Locate every uninfected red blood cell.
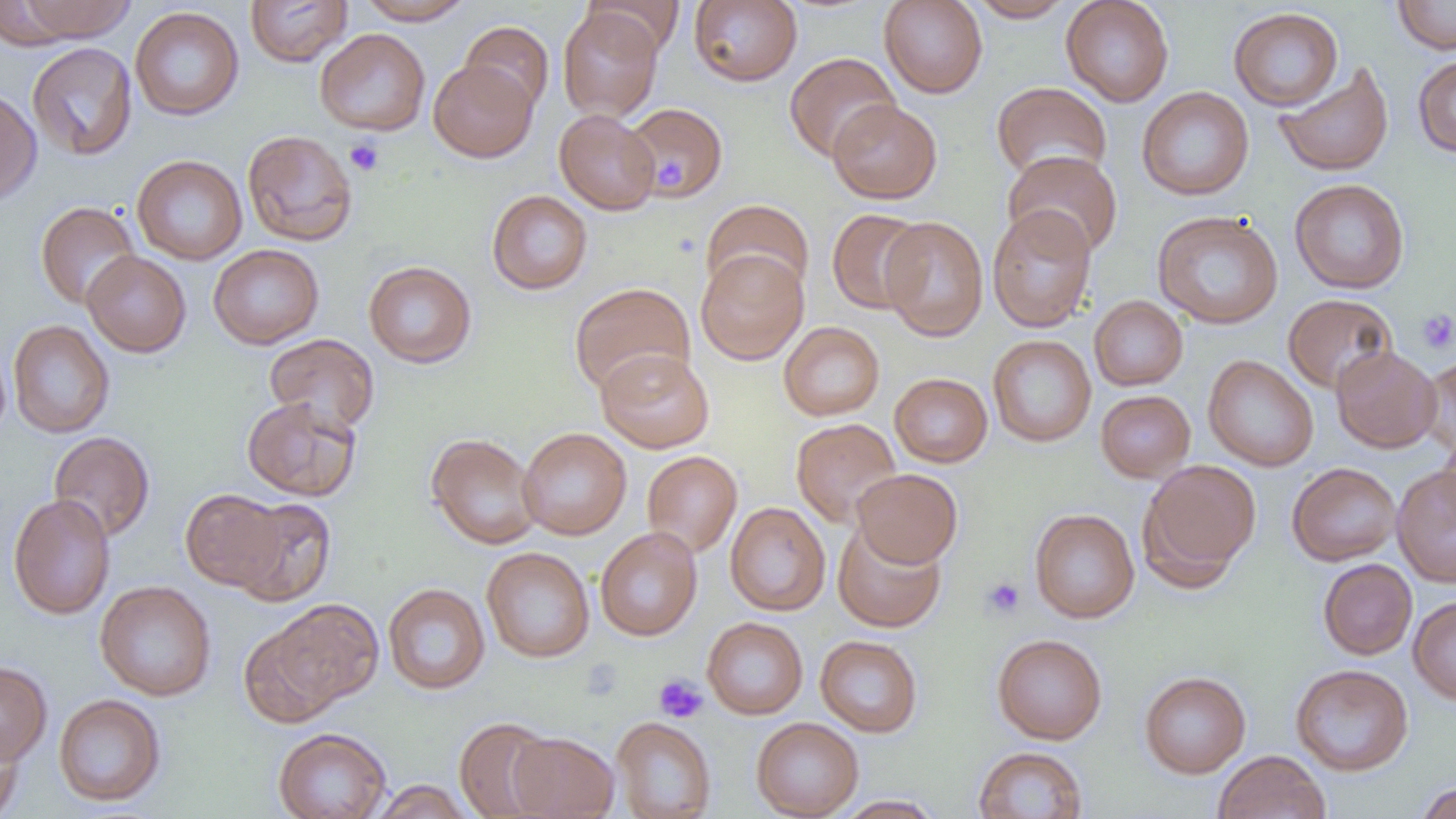

Approximate bounding boxes as named x1/y1/x2/y2 corners in pixels.
Uninfected red blood cells: (x1=13, y1=0, x2=136, y2=42), (x1=245, y1=0, x2=353, y2=67), (x1=357, y1=0, x2=475, y2=25), (x1=583, y1=0, x2=684, y2=56), (x1=688, y1=0, x2=802, y2=87), (x1=879, y1=0, x2=988, y2=99), (x1=967, y1=0, x2=1077, y2=22), (x1=1061, y1=0, x2=1174, y2=107), (x1=1392, y1=0, x2=1456, y2=54), (x1=129, y1=6, x2=244, y2=121), (x1=557, y1=6, x2=664, y2=121), (x1=1228, y1=6, x2=1344, y2=111), (x1=460, y1=20, x2=555, y2=116), (x1=315, y1=28, x2=430, y2=136), (x1=26, y1=42, x2=137, y2=161), (x1=784, y1=52, x2=901, y2=162), (x1=1412, y1=55, x2=1456, y2=157), (x1=428, y1=59, x2=538, y2=162), (x1=1274, y1=62, x2=1394, y2=177), (x1=992, y1=81, x2=1112, y2=182), (x1=1137, y1=86, x2=1254, y2=201), (x1=0, y1=88, x2=42, y2=206), (x1=828, y1=99, x2=942, y2=204), (x1=624, y1=102, x2=728, y2=201), (x1=554, y1=109, x2=661, y2=215), (x1=242, y1=130, x2=358, y2=246), (x1=1002, y1=150, x2=1123, y2=259), (x1=132, y1=155, x2=247, y2=265), (x1=1290, y1=178, x2=1410, y2=294), (x1=487, y1=190, x2=593, y2=294), (x1=700, y1=198, x2=814, y2=299), (x1=35, y1=201, x2=141, y2=310), (x1=987, y1=205, x2=1097, y2=333), (x1=826, y1=208, x2=928, y2=315), (x1=1152, y1=210, x2=1283, y2=329), (x1=879, y1=216, x2=989, y2=342), (x1=209, y1=244, x2=324, y2=349), (x1=696, y1=249, x2=808, y2=364), (x1=81, y1=251, x2=192, y2=357), (x1=363, y1=260, x2=477, y2=368), (x1=569, y1=282, x2=695, y2=396), (x1=1282, y1=293, x2=1398, y2=394), (x1=1089, y1=295, x2=1188, y2=390), (x1=8, y1=320, x2=115, y2=438), (x1=779, y1=321, x2=885, y2=420), (x1=264, y1=333, x2=380, y2=434), (x1=988, y1=335, x2=1096, y2=447), (x1=1331, y1=345, x2=1441, y2=453), (x1=596, y1=348, x2=714, y2=453), (x1=1203, y1=355, x2=1318, y2=471), (x1=1417, y1=355, x2=1456, y2=459), (x1=889, y1=373, x2=992, y2=467), (x1=1095, y1=390, x2=1196, y2=483), (x1=241, y1=396, x2=362, y2=501), (x1=790, y1=418, x2=902, y2=528), (x1=518, y1=427, x2=632, y2=540), (x1=1437, y1=429, x2=1456, y2=530), (x1=48, y1=431, x2=155, y2=541), (x1=425, y1=433, x2=543, y2=550), (x1=641, y1=451, x2=742, y2=558), (x1=1138, y1=458, x2=1260, y2=589), (x1=1286, y1=462, x2=1401, y2=566), (x1=1392, y1=464, x2=1456, y2=587), (x1=852, y1=468, x2=963, y2=568), (x1=181, y1=489, x2=287, y2=591), (x1=8, y1=493, x2=116, y2=620), (x1=230, y1=498, x2=337, y2=605), (x1=725, y1=501, x2=831, y2=616), (x1=1029, y1=508, x2=1140, y2=624), (x1=832, y1=521, x2=946, y2=633), (x1=595, y1=527, x2=702, y2=641), (x1=481, y1=546, x2=595, y2=663), (x1=1318, y1=558, x2=1417, y2=659), (x1=95, y1=580, x2=216, y2=701), (x1=383, y1=583, x2=491, y2=695), (x1=1408, y1=596, x2=1456, y2=705), (x1=269, y1=598, x2=385, y2=709), (x1=702, y1=617, x2=809, y2=719), (x1=239, y1=625, x2=340, y2=729), (x1=992, y1=634, x2=1107, y2=744), (x1=815, y1=635, x2=923, y2=737), (x1=0, y1=660, x2=52, y2=766), (x1=1290, y1=664, x2=1414, y2=776), (x1=1139, y1=671, x2=1251, y2=778), (x1=53, y1=693, x2=166, y2=806), (x1=454, y1=716, x2=559, y2=819), (x1=611, y1=716, x2=716, y2=818), (x1=751, y1=717, x2=864, y2=819), (x1=0, y1=722, x2=25, y2=818), (x1=273, y1=727, x2=392, y2=819), (x1=508, y1=731, x2=620, y2=819), (x1=972, y1=746, x2=1088, y2=819), (x1=1214, y1=750, x2=1330, y2=819), (x1=370, y1=780, x2=476, y2=818), (x1=1414, y1=781, x2=1456, y2=819), (x1=833, y1=795, x2=945, y2=818).

Platelet locations: (x1=345, y1=137, x2=384, y2=176), (x1=652, y1=152, x2=689, y2=195), (x1=1415, y1=308, x2=1456, y2=354), (x1=981, y1=577, x2=1026, y2=619), (x1=653, y1=674, x2=708, y2=724). Slide-level diagnosis: no evidence of blood parasites. One field of a larger specimen. Thin blood smear. Light microscopy. 1000x magnification. Image is 1456×819 pixels.